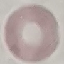 Malaria status: uninfected. Acquired by smartphone through the microscope eyepiece. Cell patch, automatically extracted from a larger field of view and resized to 64 × 64 pixels. Giemsa-stained preparation. Thin blood smear.